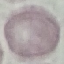

Malaria status: uninfected. Cell patch, automatically extracted from a larger field of view and resized to 64 × 64 pixels. Photographed with a smartphone camera at the microscope eyepiece. Thin smear of blood. Giemsa stain.